State which parasite is depicted.
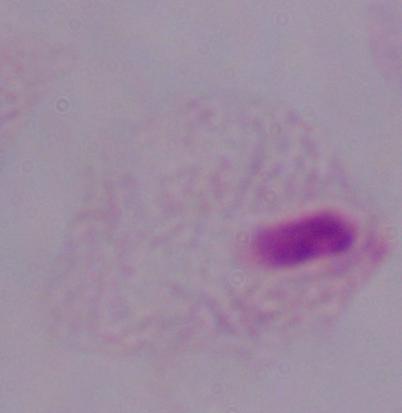

A trichomonad.

Photomicrograph. Captured at 1000x magnification.